Locate and identify every blood parasite.
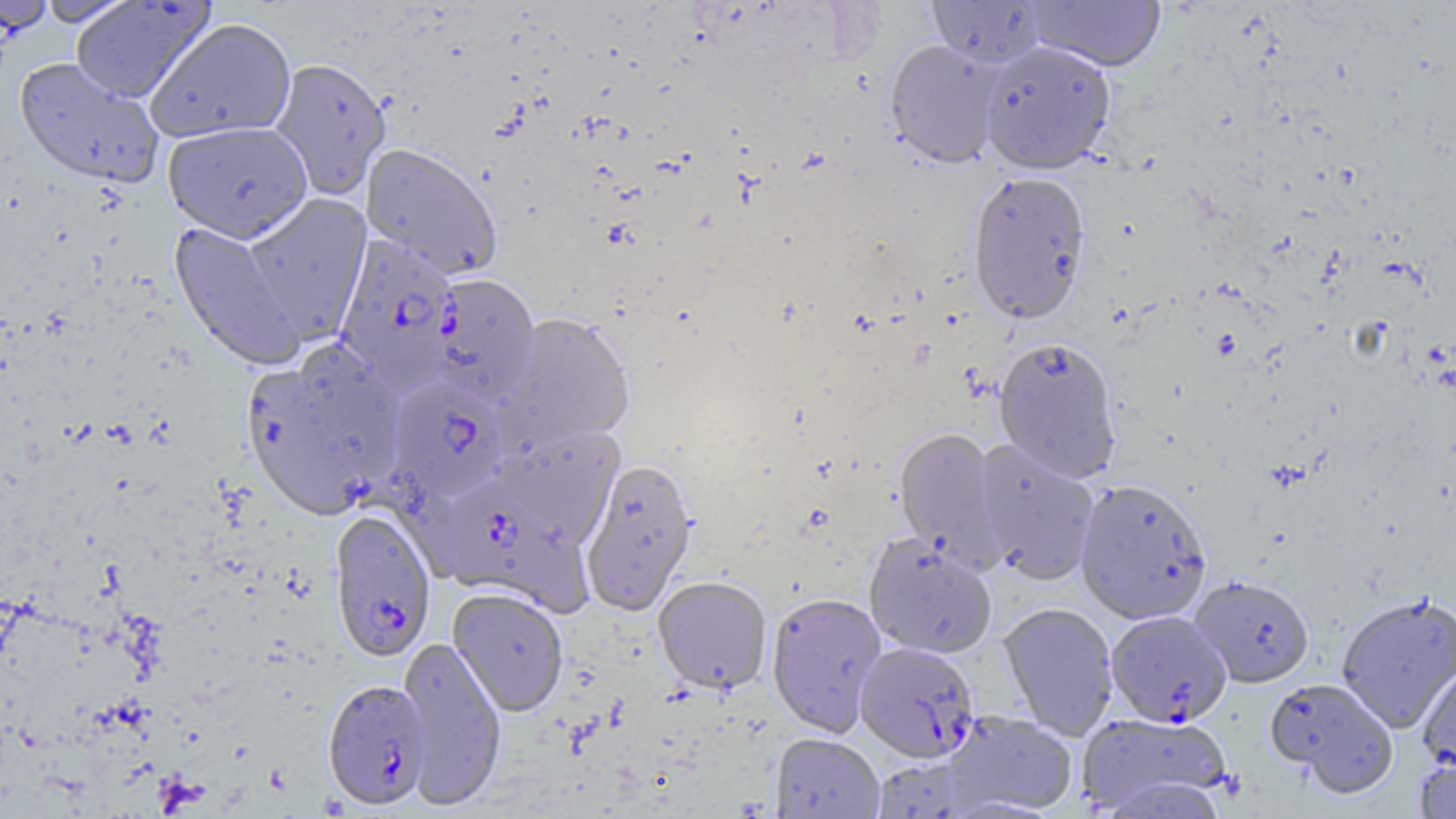
Approximate bounding boxes as (x1, y1, x2, y2) in pixels.
Plasmodium falciparum-infected red blood cells: (334, 235, 461, 393), (387, 376, 508, 502), (445, 483, 594, 618), (329, 507, 437, 663), (1108, 613, 1233, 730), (855, 641, 980, 763), (322, 678, 431, 809).
No Plasmodium ovale, Plasmodium malariae, Plasmodium vivax, Babesia divergens, or Trypanosoma brucei observed.

Summary:
  - Uninfected red blood cell locations: (0, 0, 57, 34), (71, 0, 215, 104), (927, 0, 1047, 68), (36, 1, 139, 26), (1024, 1, 1166, 72), (145, 18, 296, 143), (884, 39, 1003, 168), (978, 41, 1117, 174), (269, 57, 392, 200), (14, 58, 164, 188), (162, 120, 313, 243), (360, 144, 503, 280), (966, 170, 1092, 326), (241, 194, 372, 342), (168, 221, 305, 371), (429, 275, 541, 405), (499, 313, 635, 452), (993, 337, 1122, 483), (240, 359, 388, 517), (492, 426, 624, 546), (894, 427, 1005, 570), (972, 439, 1101, 586), (580, 459, 698, 615), (1074, 478, 1213, 624), (864, 534, 998, 660), (1190, 575, 1315, 688), (653, 577, 772, 694), (447, 587, 568, 716), (766, 592, 886, 737), (1335, 592, 1456, 733), (998, 602, 1118, 740), (396, 635, 507, 810), (1417, 661, 1456, 775), (1265, 677, 1400, 798), (943, 711, 1078, 817), (1078, 712, 1233, 815), (771, 734, 884, 819), (1414, 755, 1456, 818)
  - Slide-level diagnosis: Plasmodium falciparum
  - Magnification: 1000x
  - Preparation: thin blood film
  - Field of view: single
  - Image size: 1456×819 pixels
  - Modality: light microscopy